Name the parasite shown.
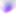

This is Toxoplasma gondii.

Photomicrograph. 400x magnification.